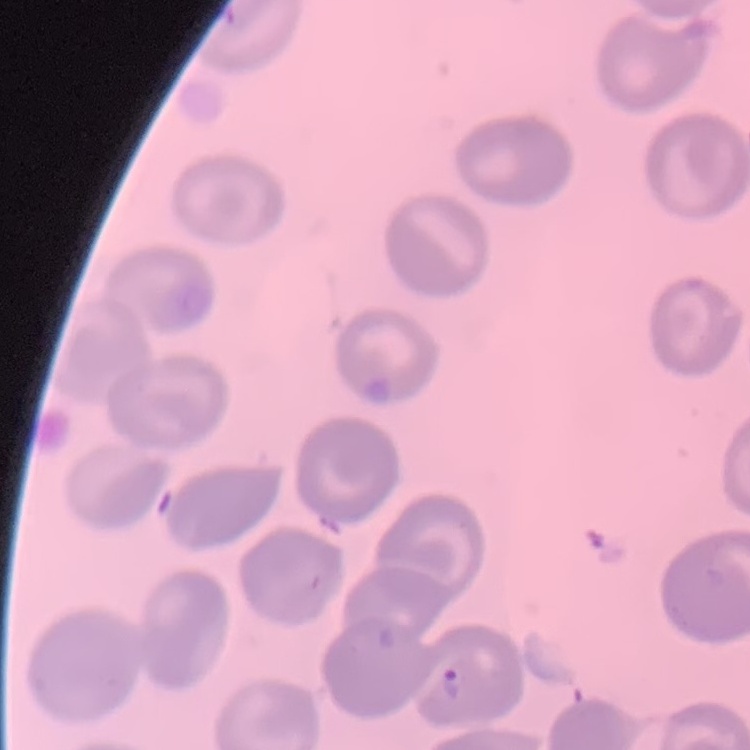

Summary:
  - Red blood cell morphology: no rouleaux formation
  - Preparation: thin blood film
  - Stain: Field's or Giemsa
  - Image type: square crop of a larger photomicrograph